Assess this cell for malaria.
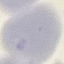

Uninfected.

stain: Giemsa
capture: smartphone through the microscope eyepiece
image_type: cell patch, automatically extracted from a larger field of view and resized to 64 × 64 pixels
preparation: thin blood film